Classify this cell by malaria status.
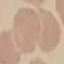

Uninfected.

Cell patch, automatically extracted from a larger field of view and resized to 64 × 64 pixels. Photographed with a smartphone camera at the microscope eyepiece. Thin smear of blood. Giemsa-stained preparation.